Locate every blood parasite and identify its species.
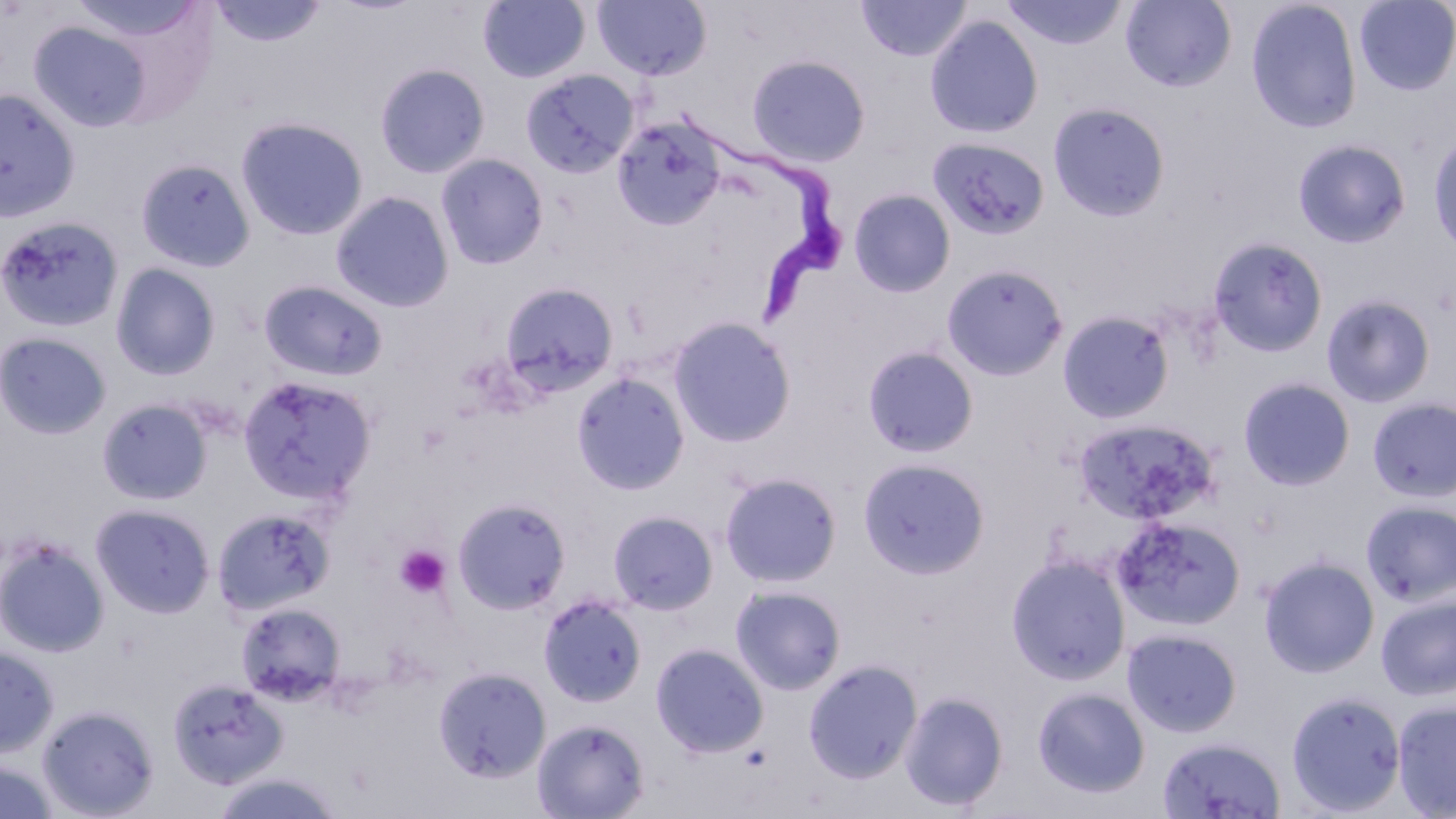
Approximate bounding boxes as (x1,y1)-(x2,y2) corner pairs in pixels.
Trypanosoma brucei: (690,117)-(849,324).
No Plasmodium falciparum, Plasmodium ovale, Plasmodium malariae, Plasmodium vivax, or Babesia divergens observed.

Uninfected red blood cell locations: (67,0)-(207,48), (208,0)-(329,48), (1120,0)-(1237,92), (478,1)-(590,83), (591,1)-(713,82), (855,1)-(972,61), (1001,1)-(1129,51), (1245,1)-(1362,134), (1353,1)-(1456,96), (924,14)-(1044,139), (27,18)-(159,133), (746,54)-(871,167), (374,62)-(491,179), (519,68)-(639,179), (0,87)-(81,224), (1047,101)-(1170,222), (235,115)-(369,242), (611,116)-(726,230), (1428,129)-(1456,258), (927,136)-(1051,241), (1292,138)-(1412,250), (435,153)-(549,271), (135,157)-(256,272), (848,188)-(957,298), (331,190)-(454,313), (0,215)-(125,333), (1207,236)-(1328,358), (111,262)-(222,381), (940,263)-(1069,381), (258,279)-(389,382), (499,281)-(620,397), (1321,293)-(1436,409), (1057,310)-(1175,424), (667,316)-(797,447), (0,331)-(112,440), (862,345)-(980,458), (571,370)-(691,496), (237,374)-(378,506), (1237,377)-(1356,491), (1367,396)-(1456,503), (97,397)-(214,506), (1073,416)-(1220,525), (857,457)-(991,579), (719,471)-(843,588), (453,496)-(572,614), (1360,500)-(1456,606), (90,502)-(216,618), (212,505)-(337,616), (607,510)-(719,615), (1112,515)-(1245,632), (0,535)-(110,657), (1005,553)-(1131,686), (1258,555)-(1380,679), (729,584)-(847,695), (538,593)-(648,708), (1375,593)-(1456,702), (235,601)-(346,704), (1122,628)-(1242,738), (651,642)-(769,757), (0,645)-(59,758), (803,658)-(923,784), (433,666)-(550,783), (167,676)-(288,789), (1031,686)-(1151,799), (899,690)-(1008,812), (1285,690)-(1407,816), (1392,700)-(1456,818), (36,703)-(161,818), (532,717)-(650,818), (1156,735)-(1287,819), (0,757)-(62,819), (209,770)-(347,819). Platelet locations: (394,545)-(451,598). Slide-level diagnosis: Trypanosoma brucei. May-Grünwald-Giemsa-stained preparation. Light microscopy. Captured at 1000x magnification. One field of a larger specimen. Image is 1456×819 pixels. Thin blood film.